State the blood parasite species.
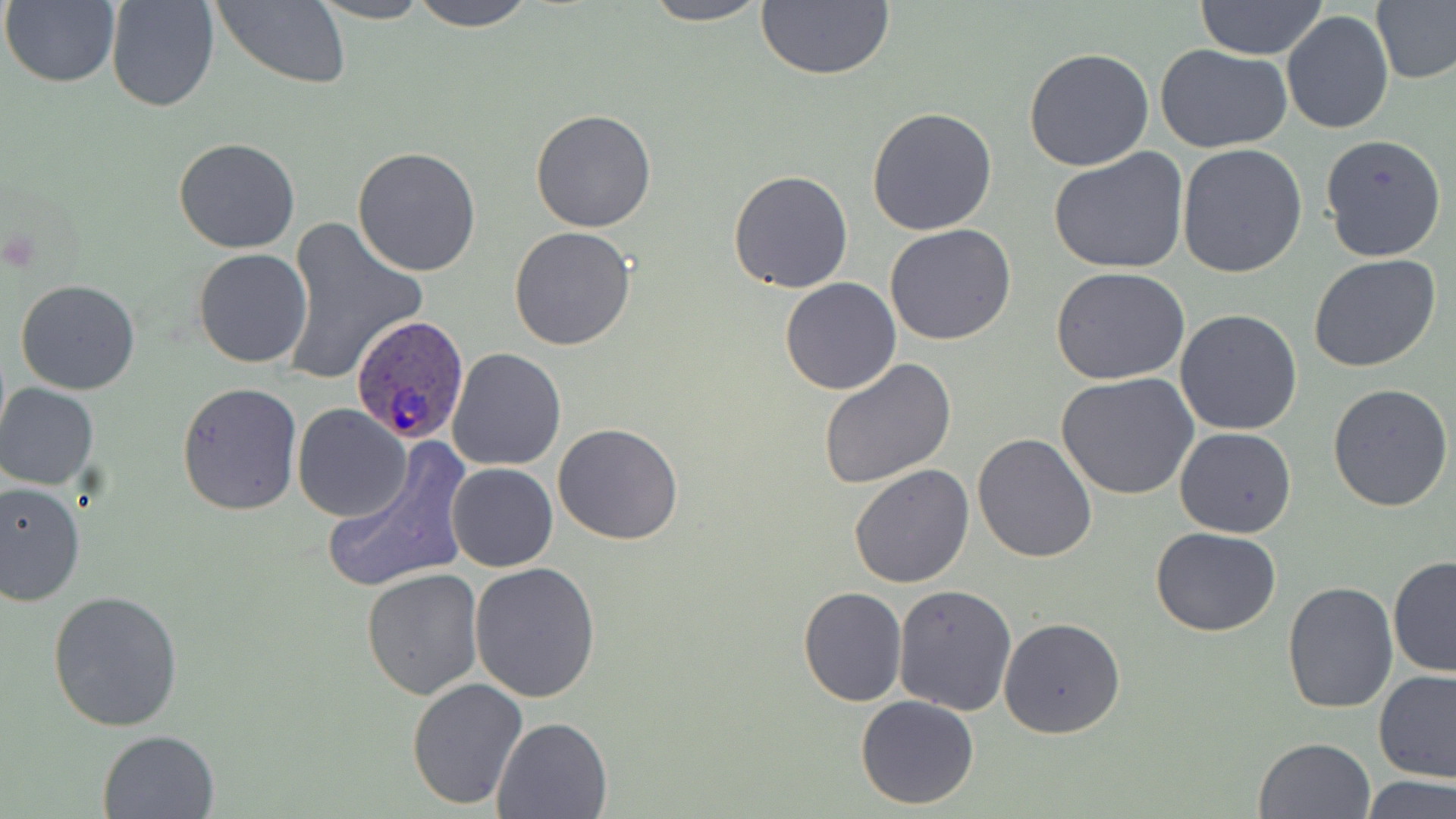

Plasmodium ovale.

Summary:
  - Coordinate format: approximate bounding boxes as [x1, y1, x2, y2] in pixels
  - Uninfected red blood cell locations: [2, 0, 121, 88], [106, 0, 219, 112], [213, 0, 350, 89], [309, 0, 434, 24], [410, 0, 537, 30], [638, 0, 773, 26], [755, 0, 896, 81], [1195, 1, 1329, 60], [1373, 1, 1456, 86], [1282, 10, 1392, 135], [1156, 44, 1293, 154], [1023, 47, 1154, 172], [866, 106, 998, 235], [531, 108, 657, 232], [1319, 134, 1447, 263], [173, 137, 300, 254], [1178, 144, 1307, 281], [352, 146, 481, 277], [1046, 148, 1190, 277], [729, 171, 854, 293], [280, 217, 429, 387], [884, 224, 1016, 347], [509, 227, 637, 349], [192, 247, 312, 368], [1308, 254, 1441, 372], [1049, 268, 1191, 386], [779, 277, 901, 396], [15, 280, 141, 395], [1174, 308, 1303, 436], [445, 347, 566, 471], [818, 357, 956, 488], [1057, 374, 1201, 502], [177, 381, 302, 515], [1, 383, 99, 490], [1328, 384, 1454, 512], [293, 404, 411, 521], [553, 422, 683, 545], [1174, 427, 1296, 538], [973, 433, 1097, 563], [321, 449, 470, 595], [446, 462, 558, 572], [848, 463, 975, 589], [0, 481, 85, 605], [1152, 526, 1279, 637], [1388, 555, 1456, 677], [470, 563, 601, 704], [361, 567, 486, 700], [1281, 581, 1399, 716], [894, 585, 1017, 716], [798, 586, 907, 705], [47, 587, 187, 731], [998, 616, 1126, 740], [1372, 669, 1456, 783], [406, 678, 529, 809], [856, 695, 981, 808], [493, 715, 613, 817], [97, 729, 220, 818], [1254, 736, 1377, 819], [1362, 776, 1455, 818]
  - Plasmodium ovale-infected red blood cell locations: [350, 315, 469, 444]
  - Image size: 1456×819 pixels
  - Field of view: one of a larger specimen
  - Preparation: thin blood film
  - Modality: optical microscopy
  - Magnification: 1000x
  - Stain: May-Grünwald-Giemsa